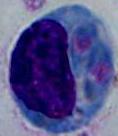

{
  "modality": "photomicrograph",
  "identification": "leukocyte",
  "magnification": "1000x"
}